Give the position of every leukocyte visible.
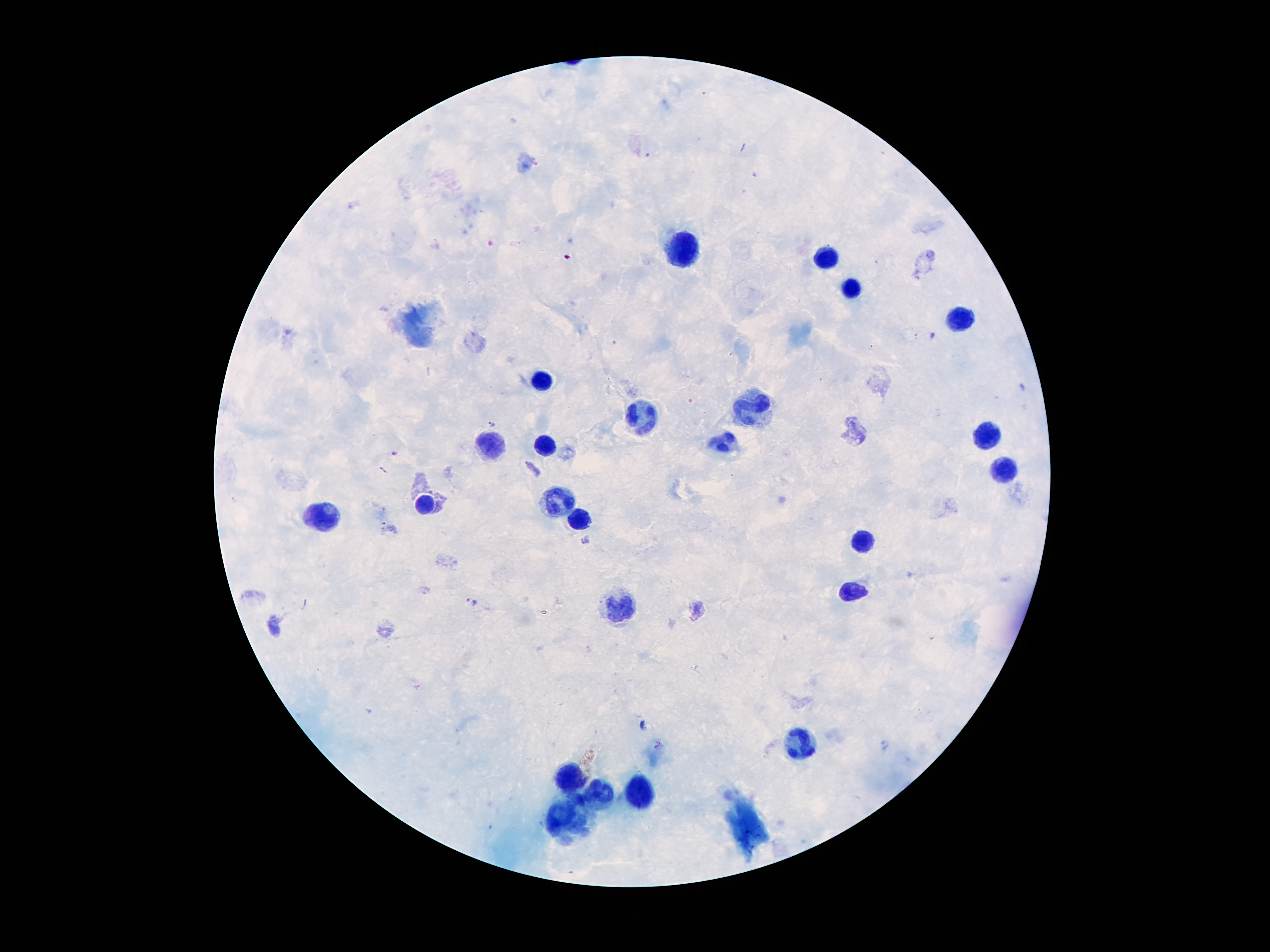

Approximate centers as [x, y] in pixels.
Leukocytes: [684, 245], [828, 257], [849, 291], [960, 320], [540, 380], [752, 405], [639, 416], [985, 441], [489, 446], [549, 449], [729, 449], [1011, 470], [556, 502], [428, 503], [325, 515], [580, 521], [863, 539], [852, 593], [620, 611], [799, 747], [567, 783], [597, 791], [640, 795], [561, 817].

Summary:
  - Plasmodium parasite locations: [754, 174], [932, 334], [493, 423], [394, 453], [586, 540], [474, 600]
  - Capture: smartphone through the microscope eyepiece
  - Patient malaria status: infected with Plasmodium falciparum
  - Preparation: thick blood film
  - Stain: Giemsa
  - Magnification: 100x
  - Image size: 1270×952 pixels
  - Field of view: one from this slide